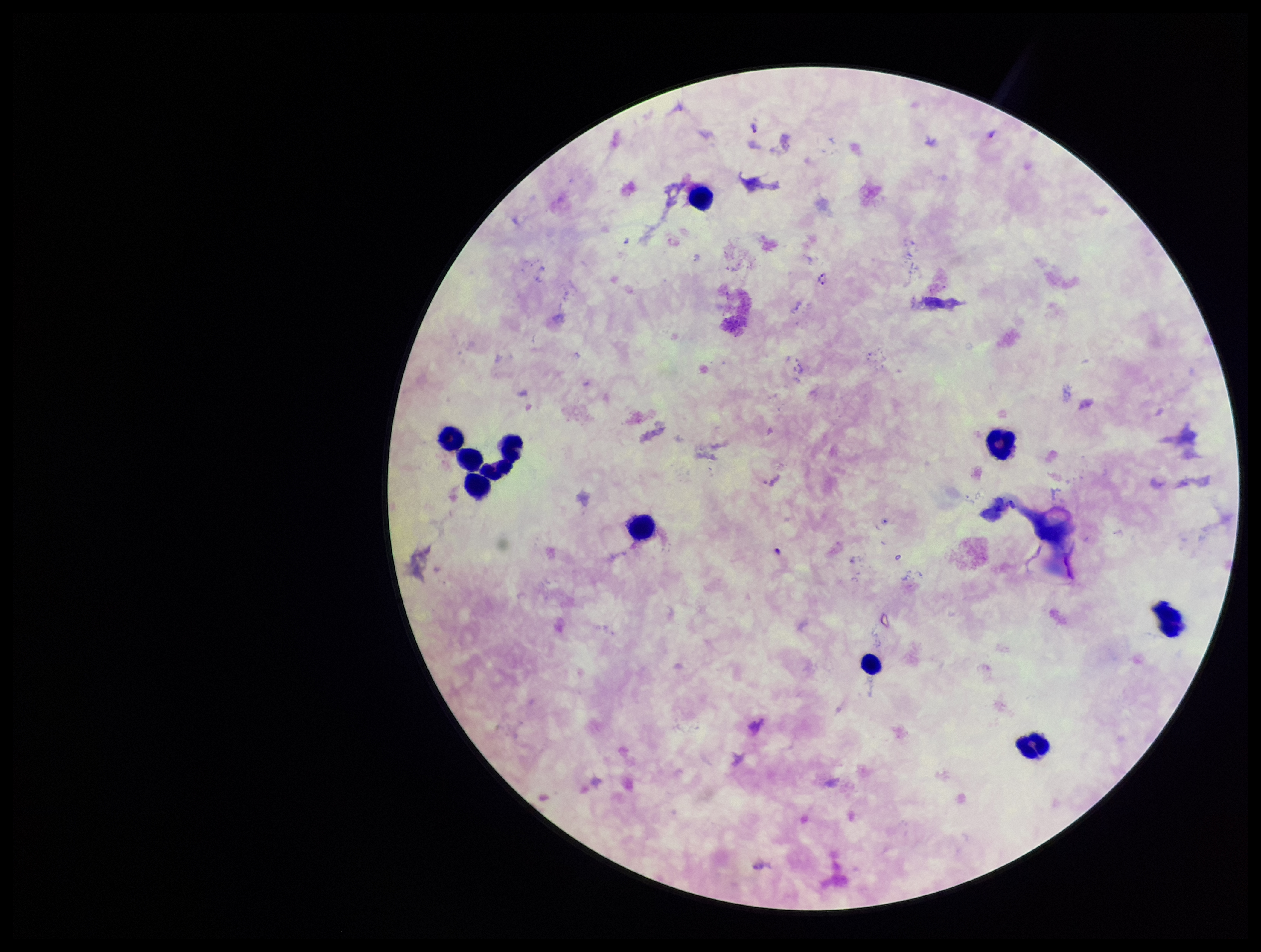
Parasite count: 2. Single field of view. Preparation: thick blood smear. Plasmodium parasites: detected. Species reported for this patient: Plasmodium falciparum. Leukocyte count: 10. Photographed through the microscope eyepiece with a smartphone camera. Giemsa stain. Image is 1261×952 pixels. Patient malaria status: positive.